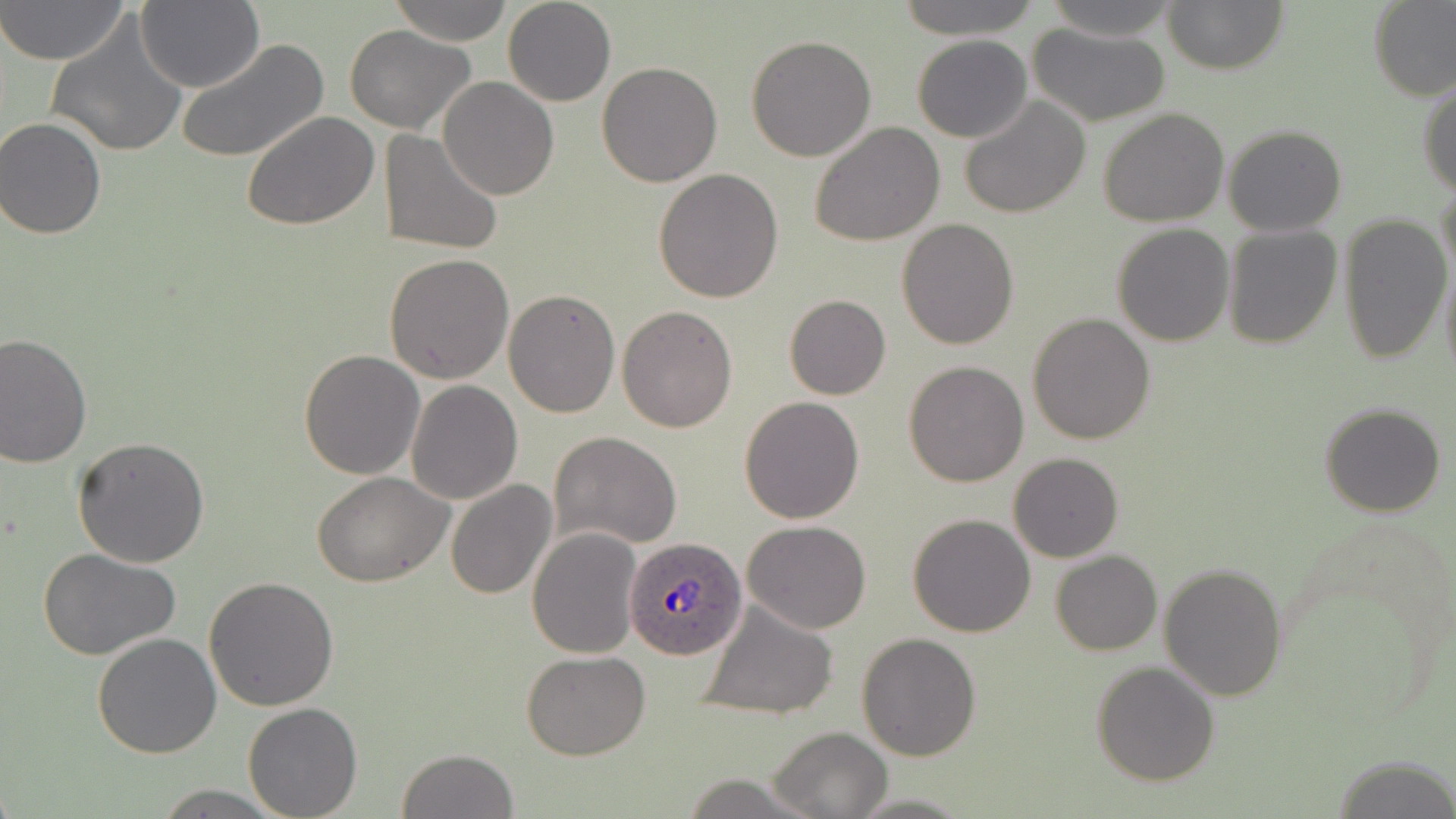

Approximate bounding boxes as named x1/y1/x2/y2 corners in pixels. Plasmodium ovale-infected red blood cell locations: (x1=624, y1=538, x2=747, y2=662). Uninfected red blood cell locations: (x1=1, y1=0, x2=129, y2=67), (x1=388, y1=0, x2=516, y2=45), (x1=503, y1=0, x2=616, y2=106), (x1=896, y1=0, x2=1039, y2=40), (x1=1040, y1=0, x2=1182, y2=42), (x1=1163, y1=1, x2=1287, y2=76), (x1=137, y1=2, x2=265, y2=91), (x1=1369, y1=2, x2=1456, y2=101), (x1=45, y1=19, x2=187, y2=159), (x1=1027, y1=23, x2=1172, y2=127), (x1=344, y1=24, x2=475, y2=133), (x1=747, y1=33, x2=876, y2=161), (x1=912, y1=35, x2=1032, y2=142), (x1=178, y1=38, x2=328, y2=164), (x1=596, y1=61, x2=724, y2=187), (x1=438, y1=77, x2=559, y2=201), (x1=1418, y1=77, x2=1456, y2=197), (x1=956, y1=94, x2=1092, y2=219), (x1=1097, y1=108, x2=1229, y2=227), (x1=241, y1=109, x2=379, y2=231), (x1=0, y1=117, x2=110, y2=239), (x1=809, y1=121, x2=947, y2=247), (x1=1222, y1=124, x2=1346, y2=236), (x1=380, y1=128, x2=504, y2=256), (x1=654, y1=168, x2=786, y2=303), (x1=1437, y1=180, x2=1456, y2=297), (x1=1337, y1=213, x2=1452, y2=365), (x1=896, y1=219, x2=1020, y2=351), (x1=1112, y1=224, x2=1235, y2=347), (x1=1222, y1=225, x2=1343, y2=350), (x1=386, y1=253, x2=513, y2=385), (x1=1438, y1=255, x2=1456, y2=385), (x1=503, y1=289, x2=620, y2=418), (x1=785, y1=294, x2=890, y2=401), (x1=617, y1=304, x2=739, y2=432), (x1=1026, y1=312, x2=1156, y2=445), (x1=0, y1=334, x2=93, y2=468), (x1=298, y1=350, x2=425, y2=481), (x1=903, y1=360, x2=1030, y2=487), (x1=406, y1=380, x2=524, y2=504), (x1=738, y1=395, x2=865, y2=523), (x1=1318, y1=403, x2=1448, y2=517), (x1=548, y1=431, x2=684, y2=550), (x1=71, y1=436, x2=210, y2=570), (x1=1009, y1=452, x2=1123, y2=562), (x1=313, y1=472, x2=454, y2=588), (x1=446, y1=479, x2=558, y2=601), (x1=907, y1=514, x2=1036, y2=637), (x1=742, y1=520, x2=872, y2=634), (x1=527, y1=528, x2=642, y2=660), (x1=37, y1=547, x2=186, y2=663), (x1=729, y1=550, x2=865, y2=689), (x1=1050, y1=550, x2=1162, y2=656), (x1=1159, y1=563, x2=1288, y2=701), (x1=204, y1=575, x2=339, y2=710), (x1=697, y1=599, x2=839, y2=720), (x1=856, y1=631, x2=982, y2=760), (x1=92, y1=632, x2=222, y2=758), (x1=522, y1=649, x2=651, y2=760), (x1=1091, y1=661, x2=1221, y2=786), (x1=242, y1=702, x2=363, y2=818), (x1=768, y1=726, x2=893, y2=819), (x1=396, y1=748, x2=519, y2=819), (x1=1336, y1=757, x2=1454, y2=818). Slide-level diagnosis: Plasmodium ovale. Single field of view. Optical microscopy. Thin blood smear. May-Grünwald-Giemsa-stained preparation. Image is 1456×819 pixels. Captured at 1000x magnification.